Comment on the morphology of the erythrocytes.
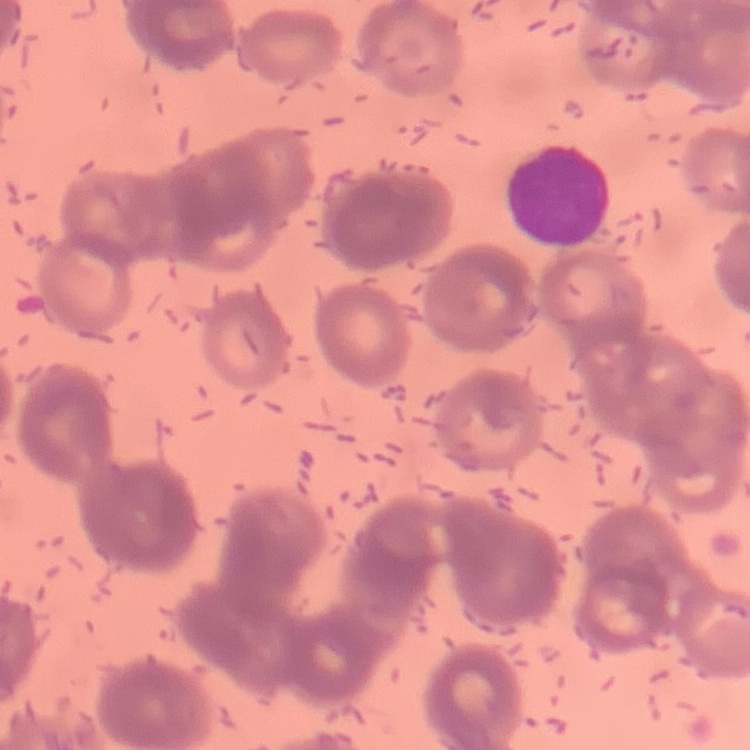

Rouleaux formation.

Summary:
  - Preparation: thin blood film
  - Image type: one tile cut from a larger photomicrograph
  - Stain: Field's or Giemsa